Assess this cell for malaria.
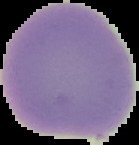

It is uninfected.

{
  "preparation": "thin blood smear",
  "image_type": "segmented cell region with the area outside set to black",
  "image_size": "139×145 pixels"
}